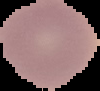
Summary:
  - Preparation: thin blood smear
  - Image size: 100×91 pixels
  - Image type: segmented cell region with the area outside set to black
  - Malaria status: uninfected